Assess this cell for malaria.
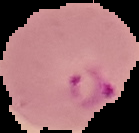

Parasitized.

Image is 139×133 pixels. From a thin blood film. Segmented cell region on a black background.